Locate every Plasmodium parasite.
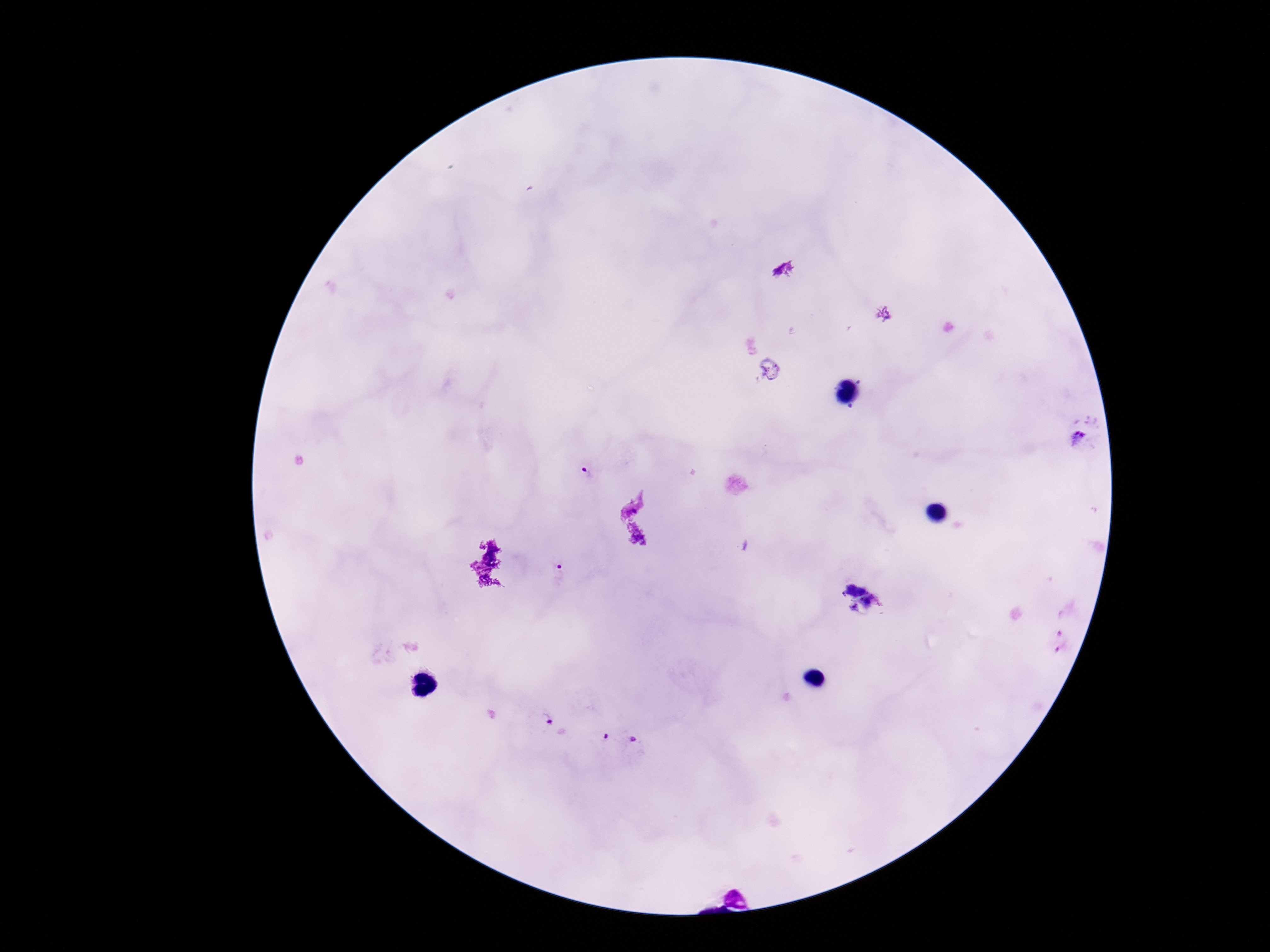

Approximate centers as [x, y] in pixels.
Plasmodium parasites: [1084, 437], [586, 470], [558, 568], [549, 723], [606, 737], [634, 739].

patient_malaria_status: positive
stain: Giemsa
image_size: 1270×952 pixels
preparation: thick blood smear
magnification: 100x
field_of_view: single
capture: smartphone camera through the microscope eyepiece